State which parasite is depicted.
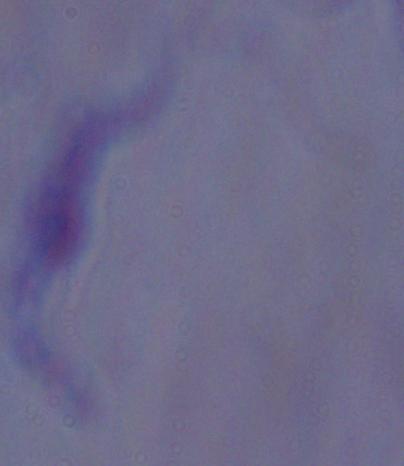

This is a trypanosome.

1000x magnification. Micrograph.